Identify the preparation type.
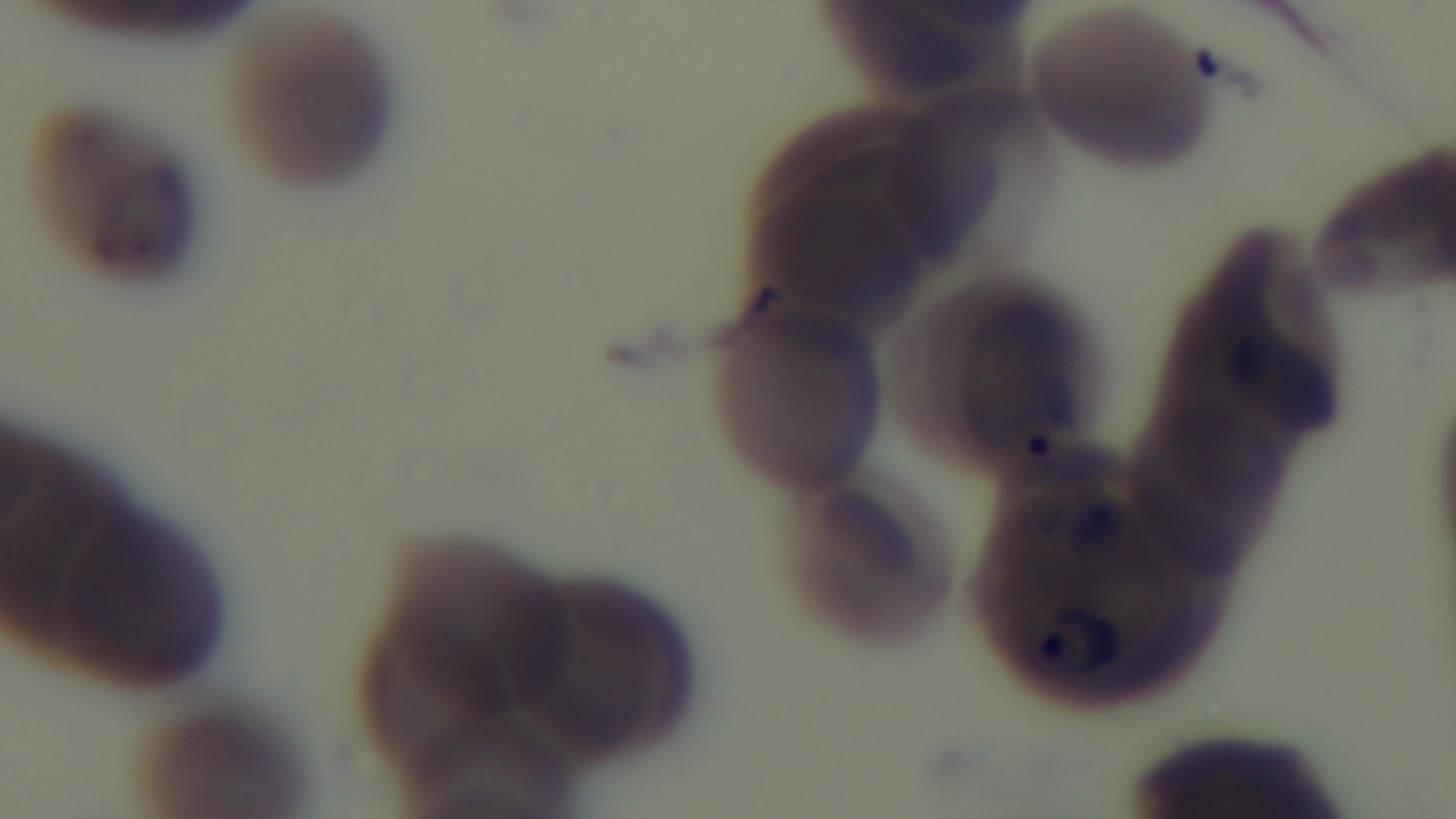
A thin smear.

capture = mounted 4K digital camera
field of view = single
objective = 100x oil immersion
malaria status = infected
modality = light microscopy
stain = Giemsa